Give the position of every leukocyte visible.
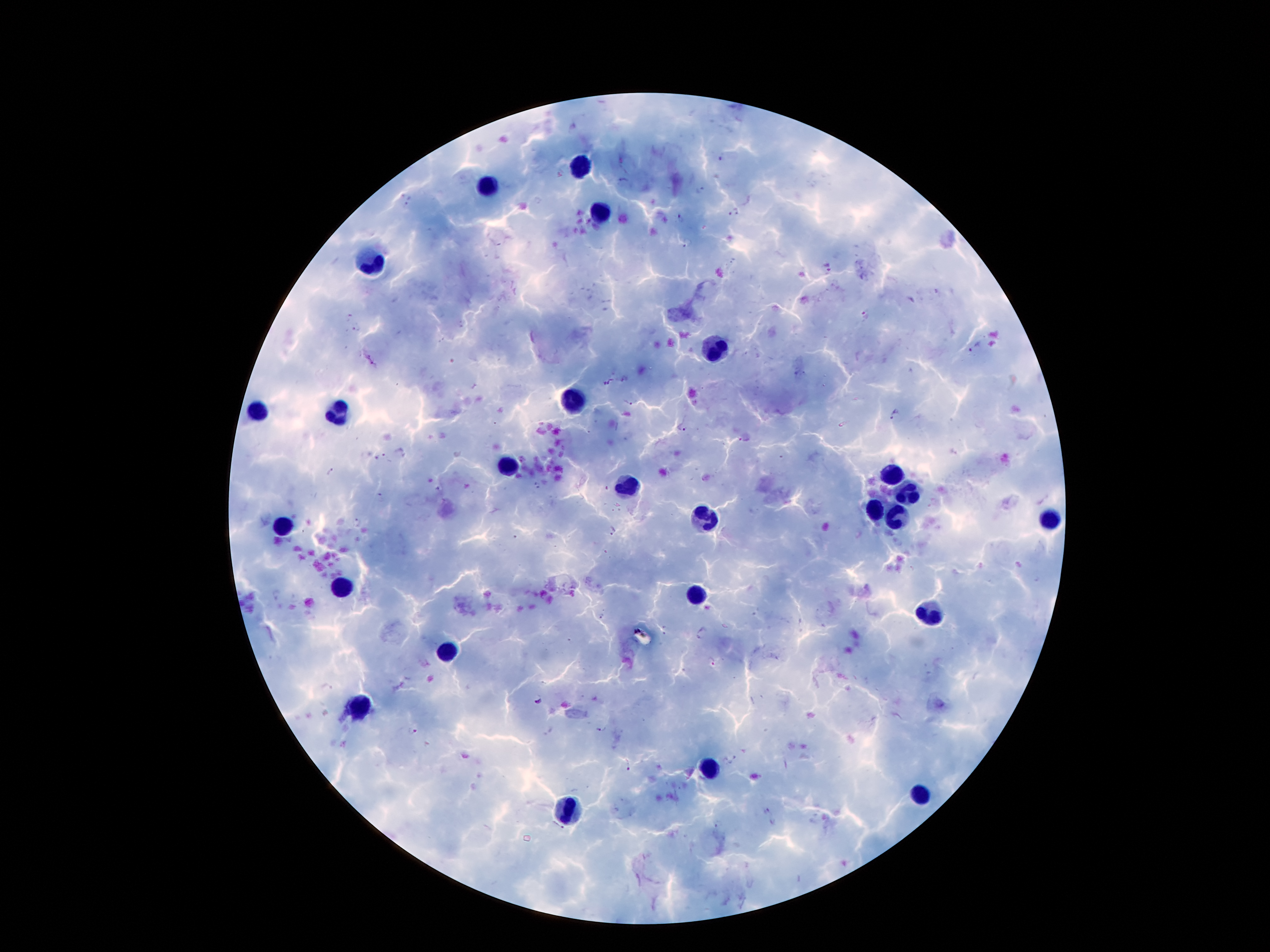
Approximate centers as {x, y} in pixels.
Leukocytes: {579, 164}, {491, 183}, {595, 214}, {372, 259}, {710, 345}, {573, 402}, {255, 408}, {337, 412}, {507, 465}, {890, 474}, {626, 482}, {909, 492}, {878, 513}, {704, 517}, {890, 521}, {1050, 521}, {282, 527}, {348, 584}, {698, 596}, {931, 611}, {444, 650}, {362, 705}, {706, 768}, {919, 793}, {569, 811}.

Summary:
  - Malaria parasite locations: {718, 158}, {622, 182}, {701, 190}, {406, 203}, {735, 211}, {680, 218}, {687, 243}, {829, 267}, {864, 314}, {348, 316}, {358, 327}, {975, 346}, {610, 383}, {628, 404}, {894, 415}, {685, 429}, {739, 441}, {400, 452}, {380, 456}, {332, 472}, {535, 485}, {379, 494}, {358, 522}, {613, 531}, {601, 617}, {665, 630}, {702, 633}, {712, 663}, {539, 700}, {412, 730}, {733, 760}, {628, 766}, {765, 811}, {773, 823}, {555, 829}
  - Image size: 1270×952 pixels
  - Stain: Giemsa
  - Preparation: thick blood film
  - Field of view: one from this slide
  - Patient malaria status: positive for Plasmodium falciparum
  - Magnification: 100x
  - Capture: smartphone through the microscope eyepiece